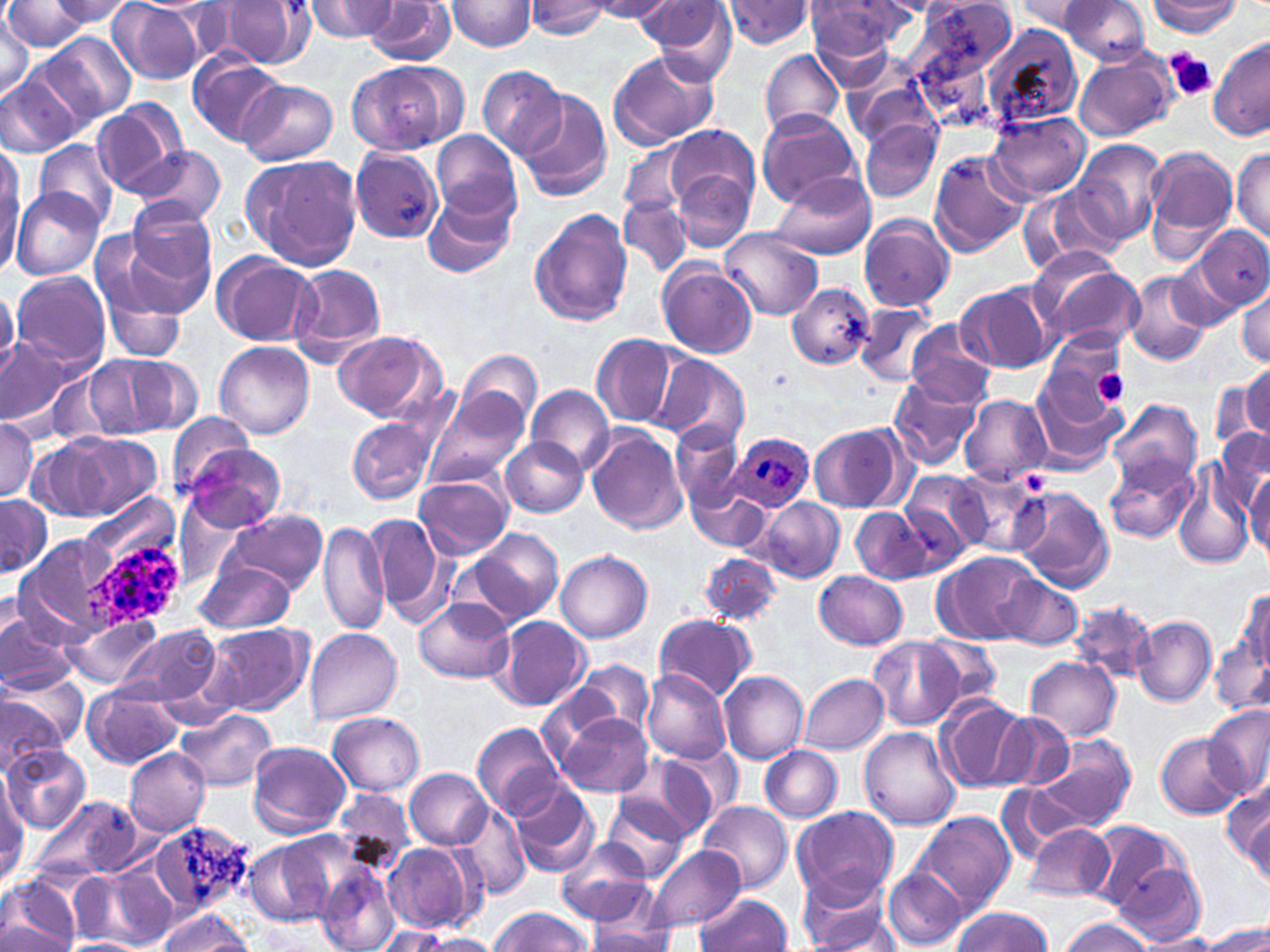
slide-level diagnosis = Plasmodium ovale
magnification = 1000x
uninfected red blood cell locations = approximate bounding boxes as named x1/y1/x2/y2 corners in pixels: (x1=43, y1=0, x2=138, y2=29), (x1=109, y1=0, x2=205, y2=84), (x1=307, y1=0, x2=399, y2=41), (x1=641, y1=0, x2=741, y2=76), (x1=722, y1=0, x2=816, y2=48), (x1=1061, y1=0, x2=1151, y2=66), (x1=211, y1=1, x2=313, y2=69), (x1=445, y1=1, x2=537, y2=52), (x1=527, y1=1, x2=611, y2=38), (x1=583, y1=1, x2=678, y2=21), (x1=909, y1=1, x2=1013, y2=97), (x1=1016, y1=1, x2=1103, y2=36), (x1=1145, y1=1, x2=1241, y2=36), (x1=2, y1=2, x2=96, y2=52), (x1=363, y1=2, x2=457, y2=65), (x1=808, y1=3, x2=898, y2=70), (x1=0, y1=11, x2=35, y2=100), (x1=983, y1=26, x2=1083, y2=131), (x1=35, y1=32, x2=135, y2=126), (x1=1210, y1=38, x2=1270, y2=142), (x1=758, y1=49, x2=844, y2=139), (x1=606, y1=50, x2=720, y2=152), (x1=187, y1=52, x2=288, y2=146), (x1=1075, y1=52, x2=1176, y2=142), (x1=346, y1=59, x2=463, y2=156), (x1=476, y1=64, x2=567, y2=159), (x1=1, y1=66, x2=90, y2=157), (x1=848, y1=74, x2=938, y2=151), (x1=237, y1=79, x2=338, y2=166), (x1=514, y1=87, x2=611, y2=202), (x1=90, y1=98, x2=189, y2=199), (x1=758, y1=109, x2=861, y2=207), (x1=983, y1=112, x2=1091, y2=203), (x1=860, y1=121, x2=940, y2=201), (x1=664, y1=123, x2=759, y2=217), (x1=431, y1=130, x2=521, y2=223), (x1=33, y1=139, x2=119, y2=231), (x1=1076, y1=139, x2=1167, y2=246), (x1=619, y1=143, x2=690, y2=216), (x1=132, y1=146, x2=224, y2=223), (x1=1, y1=148, x2=23, y2=267), (x1=350, y1=148, x2=443, y2=243), (x1=1144, y1=148, x2=1238, y2=261), (x1=1232, y1=148, x2=1270, y2=243), (x1=928, y1=151, x2=1029, y2=255), (x1=243, y1=153, x2=362, y2=270), (x1=768, y1=170, x2=877, y2=261), (x1=674, y1=172, x2=752, y2=251), (x1=1026, y1=185, x2=1124, y2=275), (x1=12, y1=187, x2=102, y2=280), (x1=422, y1=188, x2=516, y2=280), (x1=620, y1=196, x2=691, y2=275), (x1=528, y1=208, x2=633, y2=328), (x1=120, y1=211, x2=217, y2=317), (x1=858, y1=214, x2=954, y2=311), (x1=1194, y1=225, x2=1270, y2=309), (x1=722, y1=228, x2=824, y2=321), (x1=91, y1=240, x2=193, y2=353), (x1=211, y1=253, x2=318, y2=347), (x1=1168, y1=254, x2=1245, y2=331), (x1=657, y1=259, x2=758, y2=360), (x1=1034, y1=263, x2=1143, y2=355), (x1=288, y1=264, x2=386, y2=365), (x1=10, y1=271, x2=111, y2=367), (x1=1124, y1=271, x2=1211, y2=366), (x1=955, y1=281, x2=1058, y2=374), (x1=787, y1=282, x2=874, y2=370), (x1=1236, y1=287, x2=1270, y2=368), (x1=855, y1=303, x2=936, y2=386), (x1=906, y1=321, x2=994, y2=404), (x1=331, y1=329, x2=444, y2=423), (x1=0, y1=333, x2=90, y2=434), (x1=592, y1=333, x2=675, y2=427), (x1=1044, y1=333, x2=1128, y2=411), (x1=214, y1=341, x2=314, y2=438), (x1=461, y1=350, x2=542, y2=429), (x1=444, y1=354, x2=571, y2=462), (x1=653, y1=354, x2=750, y2=450), (x1=89, y1=356, x2=197, y2=438), (x1=1242, y1=362, x2=1270, y2=441), (x1=887, y1=373, x2=984, y2=469), (x1=1211, y1=377, x2=1263, y2=450), (x1=1026, y1=379, x2=1123, y2=473), (x1=528, y1=384, x2=614, y2=474), (x1=424, y1=389, x2=528, y2=490), (x1=959, y1=395, x2=1050, y2=484), (x1=1104, y1=400, x2=1201, y2=488), (x1=168, y1=411, x2=256, y2=497), (x1=0, y1=417, x2=38, y2=502), (x1=348, y1=418, x2=434, y2=503), (x1=672, y1=419, x2=744, y2=511), (x1=807, y1=421, x2=912, y2=513), (x1=585, y1=427, x2=688, y2=535), (x1=1214, y1=429, x2=1269, y2=503), (x1=68, y1=435, x2=160, y2=518), (x1=500, y1=436, x2=588, y2=518), (x1=29, y1=441, x2=114, y2=519), (x1=182, y1=445, x2=284, y2=529), (x1=1107, y1=455, x2=1199, y2=543), (x1=1172, y1=462, x2=1255, y2=572), (x1=950, y1=468, x2=1050, y2=558), (x1=1246, y1=469, x2=1270, y2=560), (x1=903, y1=472, x2=985, y2=554), (x1=414, y1=475, x2=512, y2=560), (x1=689, y1=481, x2=771, y2=551), (x1=1011, y1=488, x2=1113, y2=592), (x1=0, y1=496, x2=51, y2=574), (x1=753, y1=498, x2=845, y2=583), (x1=850, y1=507, x2=931, y2=584), (x1=222, y1=510, x2=326, y2=595), (x1=363, y1=513, x2=448, y2=618), (x1=321, y1=520, x2=388, y2=637), (x1=466, y1=527, x2=563, y2=625), (x1=15, y1=536, x2=122, y2=640), (x1=555, y1=550, x2=652, y2=642), (x1=934, y1=550, x2=1040, y2=645), (x1=697, y1=551, x2=782, y2=626), (x1=197, y1=562, x2=297, y2=633), (x1=814, y1=570, x2=907, y2=649), (x1=999, y1=573, x2=1083, y2=651), (x1=1233, y1=589, x2=1268, y2=677), (x1=415, y1=598, x2=514, y2=685), (x1=1069, y1=599, x2=1153, y2=686), (x1=0, y1=605, x2=80, y2=691), (x1=63, y1=613, x2=161, y2=688), (x1=653, y1=614, x2=755, y2=701), (x1=1131, y1=616, x2=1216, y2=708), (x1=493, y1=617, x2=591, y2=710), (x1=203, y1=623, x2=311, y2=717), (x1=117, y1=627, x2=220, y2=709), (x1=304, y1=628, x2=402, y2=725), (x1=920, y1=635, x2=1000, y2=708), (x1=868, y1=636, x2=963, y2=730), (x1=1211, y1=636, x2=1269, y2=716), (x1=1025, y1=656, x2=1121, y2=740), (x1=574, y1=660, x2=653, y2=739), (x1=3, y1=668, x2=89, y2=751), (x1=642, y1=670, x2=733, y2=764), (x1=719, y1=671, x2=808, y2=763), (x1=799, y1=674, x2=888, y2=754), (x1=83, y1=685, x2=181, y2=770), (x1=1, y1=693, x2=66, y2=774), (x1=935, y1=695, x2=1031, y2=792), (x1=1203, y1=706, x2=1269, y2=800), (x1=178, y1=707, x2=277, y2=792), (x1=551, y1=710, x2=655, y2=799), (x1=328, y1=711, x2=425, y2=795), (x1=994, y1=712, x2=1076, y2=790), (x1=473, y1=722, x2=563, y2=818), (x1=860, y1=728, x2=962, y2=832), (x1=1156, y1=733, x2=1244, y2=819), (x1=1030, y1=735, x2=1138, y2=837), (x1=660, y1=741, x2=743, y2=825), (x1=248, y1=742, x2=353, y2=837), (x1=1, y1=744, x2=89, y2=833), (x1=759, y1=744, x2=843, y2=822), (x1=123, y1=747, x2=210, y2=837), (x1=612, y1=754, x2=713, y2=844), (x1=405, y1=768, x2=494, y2=848), (x1=0, y1=774, x2=28, y2=881), (x1=508, y1=781, x2=598, y2=878), (x1=1225, y1=781, x2=1269, y2=886), (x1=32, y1=794, x2=144, y2=883), (x1=601, y1=794, x2=692, y2=883), (x1=455, y1=800, x2=531, y2=900), (x1=695, y1=800, x2=791, y2=895), (x1=793, y1=809, x2=898, y2=903), (x1=914, y1=812, x2=1017, y2=916), (x1=149, y1=818, x2=254, y2=917), (x1=1085, y1=821, x2=1192, y2=916), (x1=1023, y1=823, x2=1115, y2=902), (x1=554, y1=838, x2=654, y2=927), (x1=246, y1=840, x2=333, y2=926), (x1=384, y1=843, x2=481, y2=933), (x1=645, y1=844, x2=745, y2=935), (x1=1112, y1=858, x2=1206, y2=943), (x1=884, y1=865, x2=966, y2=950), (x1=102, y1=867, x2=177, y2=948), (x1=316, y1=867, x2=401, y2=952), (x1=2, y1=874, x2=80, y2=952), (x1=72, y1=874, x2=150, y2=943), (x1=795, y1=876, x2=899, y2=952), (x1=693, y1=893, x2=794, y2=951), (x1=489, y1=906, x2=589, y2=952), (x1=951, y1=907, x2=1053, y2=952), (x1=156, y1=908, x2=252, y2=952), (x1=1058, y1=917, x2=1154, y2=952), (x1=1, y1=920, x2=73, y2=951), (x1=1200, y1=923, x2=1270, y2=951), (x1=372, y1=926, x2=456, y2=952), (x1=586, y1=926, x2=677, y2=951), (x1=1136, y1=933, x2=1226, y2=952), (x1=416, y1=934, x2=504, y2=951), (x1=63, y1=937, x2=141, y2=951)
image size = 1270×952 pixels
field of view = one of a larger specimen
preparation = thin blood film
Plasmodium ovale-infected red blood cell locations = approximate bounding boxes as named x1/y1/x2/y2 corners in pixels: (x1=730, y1=434, x2=814, y2=512), (x1=81, y1=542, x2=184, y2=632)
modality = optical microscopy
platelet locations = approximate bounding boxes as named x1/y1/x2/y2 corners in pixels: (x1=1162, y1=49, x2=1216, y2=102), (x1=1093, y1=370, x2=1129, y2=404)
stain = May-Grünwald-Giemsa